Classify this cell by malaria status.
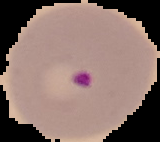

It is parasitized.

{
  "preparation": "thin blood film",
  "image_type": "cell region segmented out of the field of view; surrounding area masked to black",
  "image_size": "160×142 pixels"
}